Locate platelets.
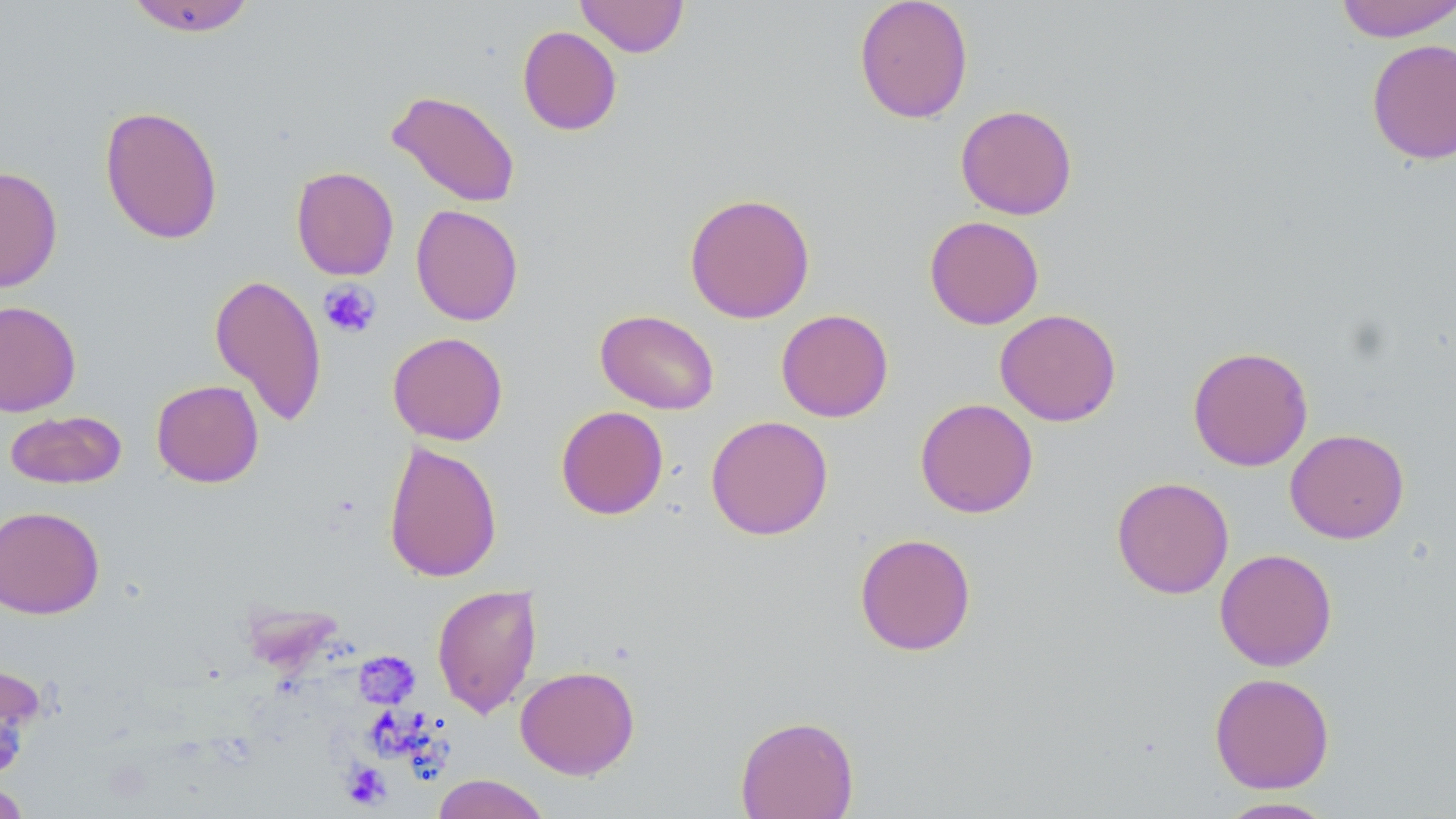

Approximate bounding boxes as (x1, y1, x2, y2) in pixels.
Platelets: (318, 280, 381, 338), (355, 651, 420, 709), (370, 706, 442, 762), (342, 762, 391, 809).

slide-level diagnosis = negative for blood parasites
modality = optical microscopy
uninfected red blood cell locations = approximate bounding boxes as (x1, y1, x2, y2) in pixels: (124, 0, 257, 37), (575, 0, 689, 57), (854, 0, 974, 124), (1334, 0, 1456, 42), (517, 25, 622, 136), (1366, 39, 1456, 164), (386, 90, 521, 208), (955, 103, 1077, 220), (99, 105, 223, 245), (0, 166, 63, 293), (291, 166, 399, 280), (684, 192, 815, 324), (410, 204, 524, 326), (924, 215, 1044, 330), (208, 273, 328, 428), (0, 300, 82, 416), (995, 308, 1122, 427), (595, 309, 720, 414), (776, 309, 893, 422), (388, 332, 508, 445), (1187, 345, 1313, 471), (151, 380, 264, 488), (914, 398, 1038, 518), (555, 405, 669, 520), (5, 409, 127, 490), (705, 415, 834, 541), (1285, 428, 1410, 543), (383, 440, 503, 583), (1111, 477, 1234, 599), (0, 504, 105, 619), (854, 532, 977, 656), (1215, 548, 1338, 671), (431, 583, 542, 719), (0, 659, 46, 780), (515, 665, 640, 779), (1209, 672, 1334, 794), (735, 715, 859, 819), (432, 774, 551, 819), (0, 782, 31, 818), (1216, 797, 1339, 818)
magnification = 1000x
field of view = one of a larger specimen
stain = May-Grünwald-Giemsa
image size = 1456×819 pixels
preparation = thin blood smear